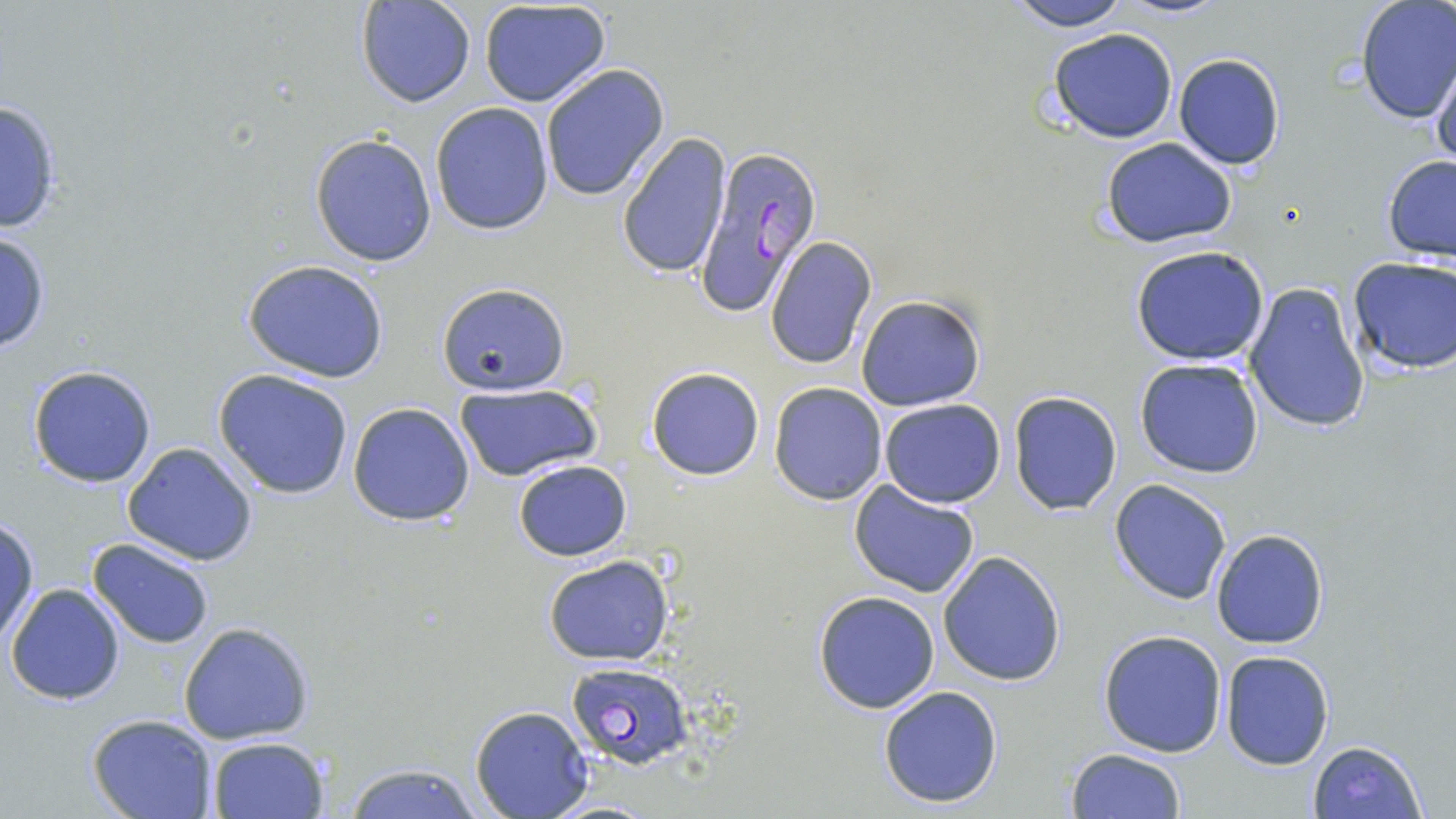

slide_level_diagnosis: Plasmodium falciparum
magnification: 1000x
uninfected_red_blood_cell_locations: 'approximate bounding boxes as [x1, y1, x2, y2] in pixels: [1002, 0, 1132, 31], [355, 1, 475, 108], [479, 2, 614, 109], [1355, 2, 1456, 124], [1046, 27, 1179, 143], [1172, 53, 1286, 171], [1430, 54, 1456, 174], [540, 64, 670, 201], [0, 96, 65, 235], [430, 101, 556, 234], [616, 131, 731, 280], [309, 132, 437, 266], [1099, 136, 1239, 248], [1382, 155, 1456, 264], [0, 230, 51, 354], [765, 237, 877, 369], [1131, 245, 1272, 366], [1349, 255, 1456, 375], [242, 259, 389, 384], [1244, 281, 1371, 436], [436, 285, 573, 396], [854, 295, 986, 410], [1134, 358, 1265, 478], [27, 364, 157, 489], [645, 367, 764, 479], [212, 368, 354, 499], [769, 382, 888, 504], [456, 386, 601, 482], [1009, 390, 1122, 514], [878, 398, 1006, 508], [348, 403, 476, 526], [121, 442, 259, 568], [514, 459, 631, 562], [1109, 480, 1231, 604], [848, 481, 982, 601], [0, 518, 38, 644], [1211, 529, 1328, 648], [86, 538, 216, 649], [938, 550, 1067, 686], [542, 555, 674, 665], [5, 583, 126, 703], [812, 590, 941, 714], [177, 622, 313, 745], [1097, 629, 1227, 757], [1220, 650, 1334, 770], [877, 685, 1005, 808], [469, 706, 594, 818], [87, 714, 218, 819], [208, 736, 328, 819], [1308, 739, 1428, 819], [1064, 749, 1186, 819], [340, 761, 485, 819]'
modality: optical microscopy
image_size: 1456×819 pixels
stain: May-Grünwald-Giemsa
preparation: thin blood smear
plasmodium_falciparum_infected_red_blood_cell_locations: 'approximate bounding boxes as [x1, y1, x2, y2] in pixels: [692, 140, 825, 317], [566, 661, 695, 769]'
field_of_view: one of a larger specimen